Locate every Plasmodium vivax-infected red blood cell.
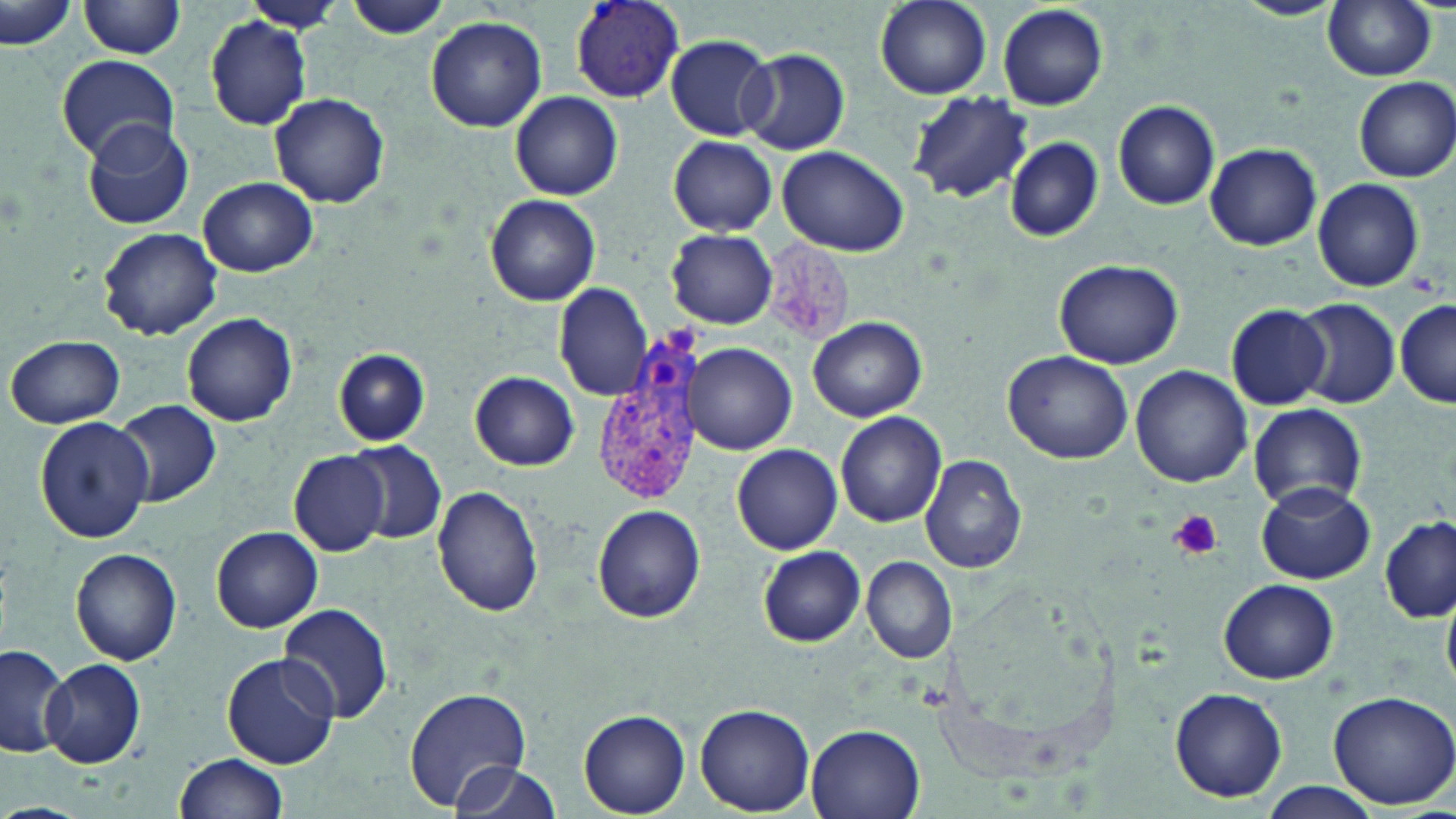

Approximate bounding boxes as [x1, y1, x2, y2] in pixels.
Plasmodium vivax-infected red blood cells: [570, 1, 687, 103], [591, 336, 709, 511].

Uninfected red blood cell locations: [875, 0, 992, 98], [1237, 0, 1339, 21], [1322, 0, 1439, 80], [80, 1, 188, 59], [239, 1, 341, 31], [342, 1, 454, 40], [1, 3, 75, 52], [995, 3, 1109, 112], [425, 15, 547, 132], [203, 16, 312, 129], [664, 33, 777, 141], [737, 48, 850, 155], [57, 54, 179, 161], [1351, 76, 1456, 183], [510, 90, 623, 201], [908, 90, 1031, 203], [269, 93, 390, 209], [1112, 100, 1222, 209], [81, 121, 193, 231], [668, 136, 777, 234], [1002, 136, 1105, 241], [1206, 142, 1322, 251], [776, 147, 910, 258], [198, 176, 320, 276], [1313, 178, 1425, 292], [485, 195, 601, 306], [97, 228, 223, 340], [666, 229, 778, 328], [1053, 257, 1184, 368], [555, 283, 654, 401], [1291, 297, 1400, 410], [1395, 297, 1455, 407], [1224, 302, 1332, 412], [182, 312, 298, 428], [809, 316, 928, 422], [7, 334, 126, 428], [688, 342, 796, 455], [335, 349, 429, 445], [1001, 351, 1133, 464], [1130, 364, 1253, 487], [469, 370, 579, 471], [112, 400, 222, 508], [1247, 404, 1368, 511], [835, 412, 947, 527], [34, 416, 153, 542], [346, 442, 446, 543], [733, 444, 842, 554], [290, 451, 389, 557], [922, 456, 1026, 572], [1258, 481, 1375, 583], [432, 485, 545, 616], [592, 503, 706, 623], [1379, 513, 1454, 622], [211, 526, 323, 633], [757, 546, 865, 646], [71, 547, 182, 665], [863, 556, 957, 664], [1218, 578, 1339, 684], [278, 604, 394, 724], [0, 643, 72, 759], [222, 652, 339, 768], [41, 658, 147, 769], [403, 684, 534, 810], [1169, 687, 1288, 802], [1325, 688, 1456, 809], [694, 704, 816, 815], [577, 709, 691, 815], [804, 722, 927, 819], [170, 752, 289, 818], [443, 758, 562, 819], [1262, 783, 1378, 817]. Platelet locations: [1167, 510, 1223, 560]. Slide-level diagnosis: Plasmodium vivax. Image is 1456×819 pixels. Captured at 1000x magnification. Optical microscopy. Thin blood film. May-Grünwald-Giemsa stain. One field of a larger specimen.